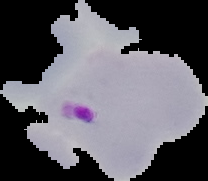
Image is 208×181 pixels. Cell region segmented out of the field of view; the surrounding area is masked to black. From a thin blood smear. Result: malaria parasites detected.